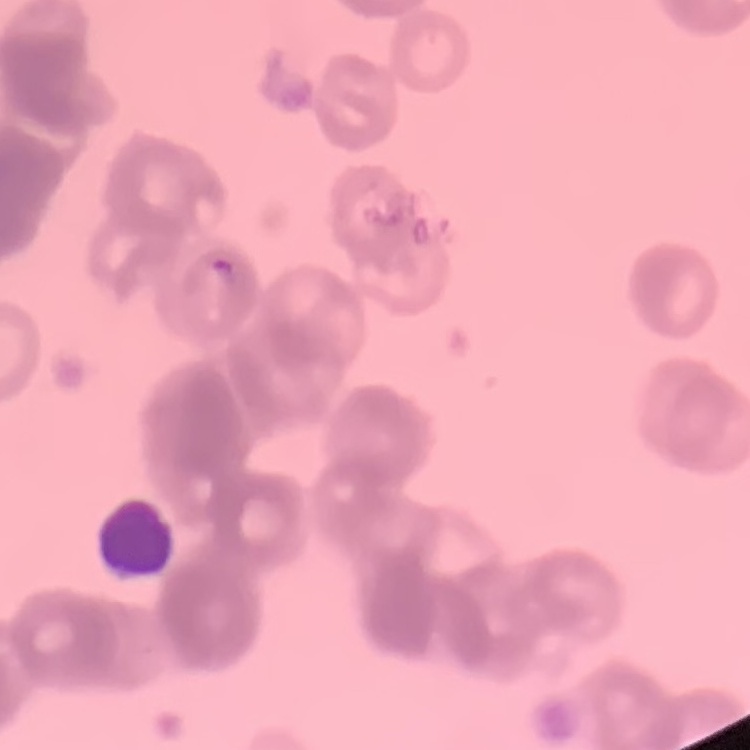 The erythrocytes show rouleaux formation. One tile cut from a larger photomicrograph. Thin blood film. Stained with either Field's or Giemsa.